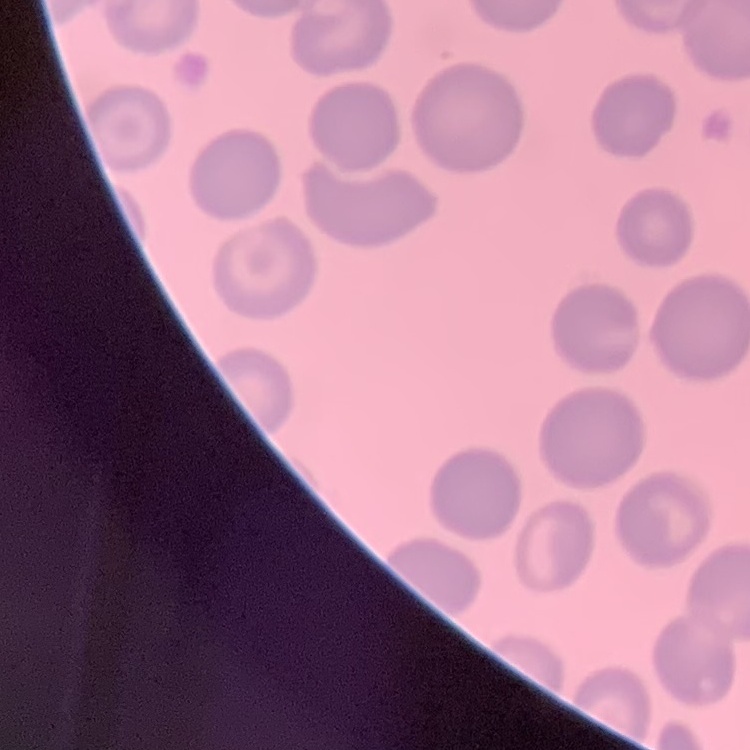
erythrocyte morphology = no rouleaux formation
image type = one tile cut from a larger photomicrograph
stain = Field's or Giemsa
preparation = thin blood smear